Outline each blood parasite and name the species.
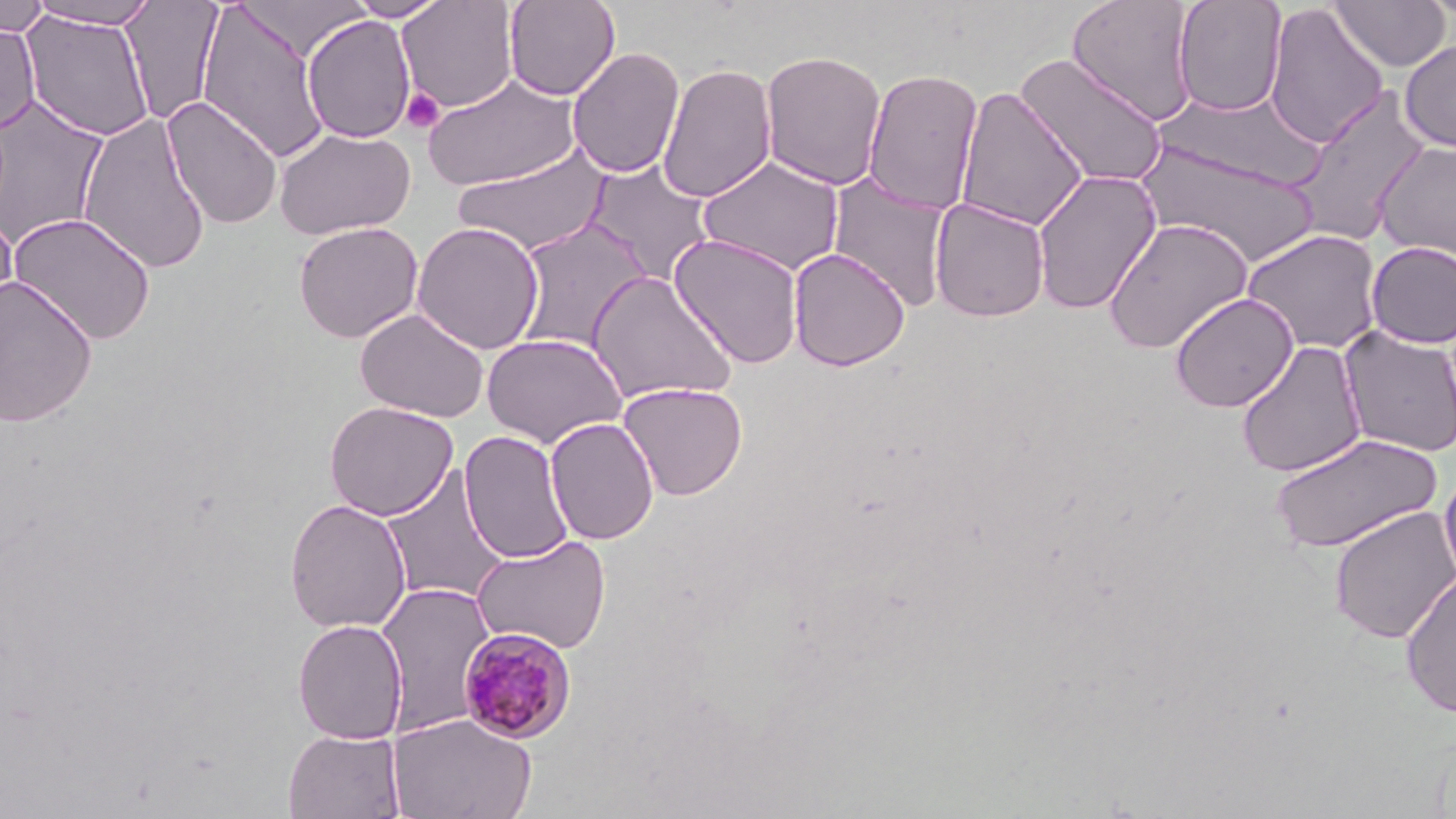
Approximate bounding boxes as [x1, y1, x2, y2] in pixels.
Plasmodium malariae-infected red blood cells: [457, 625, 577, 744].
No Plasmodium falciparum, Plasmodium ovale, Plasmodium vivax, Babesia divergens, or Trypanosoma brucei observed.

Summary:
  - Uninfected red blood cell locations: [0, 0, 50, 38], [26, 0, 161, 29], [121, 0, 224, 125], [346, 0, 450, 21], [397, 0, 519, 112], [503, 0, 620, 101], [1172, 0, 1288, 117], [1422, 0, 1455, 24], [195, 1, 332, 163], [1066, 1, 1199, 124], [1329, 1, 1451, 71], [1263, 3, 1389, 149], [20, 9, 156, 142], [301, 14, 416, 143], [0, 21, 40, 134], [1399, 40, 1456, 152], [567, 46, 685, 179], [760, 49, 887, 190], [1015, 53, 1170, 189], [657, 63, 777, 203], [862, 67, 984, 215], [421, 72, 582, 191], [954, 86, 1089, 232], [1286, 87, 1432, 247], [1157, 88, 1319, 189], [0, 95, 110, 247], [162, 96, 283, 230], [76, 112, 213, 274], [273, 127, 414, 239], [1135, 138, 1320, 267], [1373, 140, 1455, 264], [452, 145, 612, 258], [697, 155, 845, 277], [582, 160, 716, 286], [1031, 167, 1162, 315], [828, 173, 953, 313], [929, 198, 1050, 323], [0, 210, 19, 330], [8, 212, 157, 345], [1102, 217, 1254, 355], [513, 218, 652, 352], [293, 222, 424, 342], [411, 222, 545, 354], [1241, 228, 1385, 355], [669, 233, 805, 369], [1365, 241, 1456, 349], [788, 247, 910, 371], [586, 269, 738, 404], [0, 275, 98, 428], [1169, 292, 1299, 412], [354, 307, 489, 422], [1337, 326, 1456, 458], [481, 333, 627, 448], [1236, 340, 1368, 478], [618, 382, 748, 500], [324, 401, 458, 520], [545, 417, 659, 546], [459, 430, 574, 565], [1268, 433, 1442, 553], [378, 465, 511, 607], [1439, 466, 1456, 590], [284, 498, 412, 634], [1329, 505, 1456, 644], [471, 535, 611, 655], [1400, 571, 1456, 720], [374, 582, 495, 735], [292, 619, 408, 743], [388, 713, 537, 819], [282, 728, 406, 818]
  - Platelet locations: [401, 88, 445, 133]
  - Slide-level diagnosis: Plasmodium malariae
  - Modality: light microscopy
  - Magnification: 1000x
  - Preparation: thin blood smear
  - Stain: May-Grünwald-Giemsa
  - Field of view: one of a larger specimen
  - Image size: 1456×819 pixels